Assess this cell for malaria.
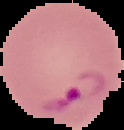
It is parasitized.

Summary:
  - Preparation: thin blood smear
  - Image type: cell region segmented out of the field of view; surrounding area masked to black
  - Image size: 124×130 pixels